State the blood parasite species.
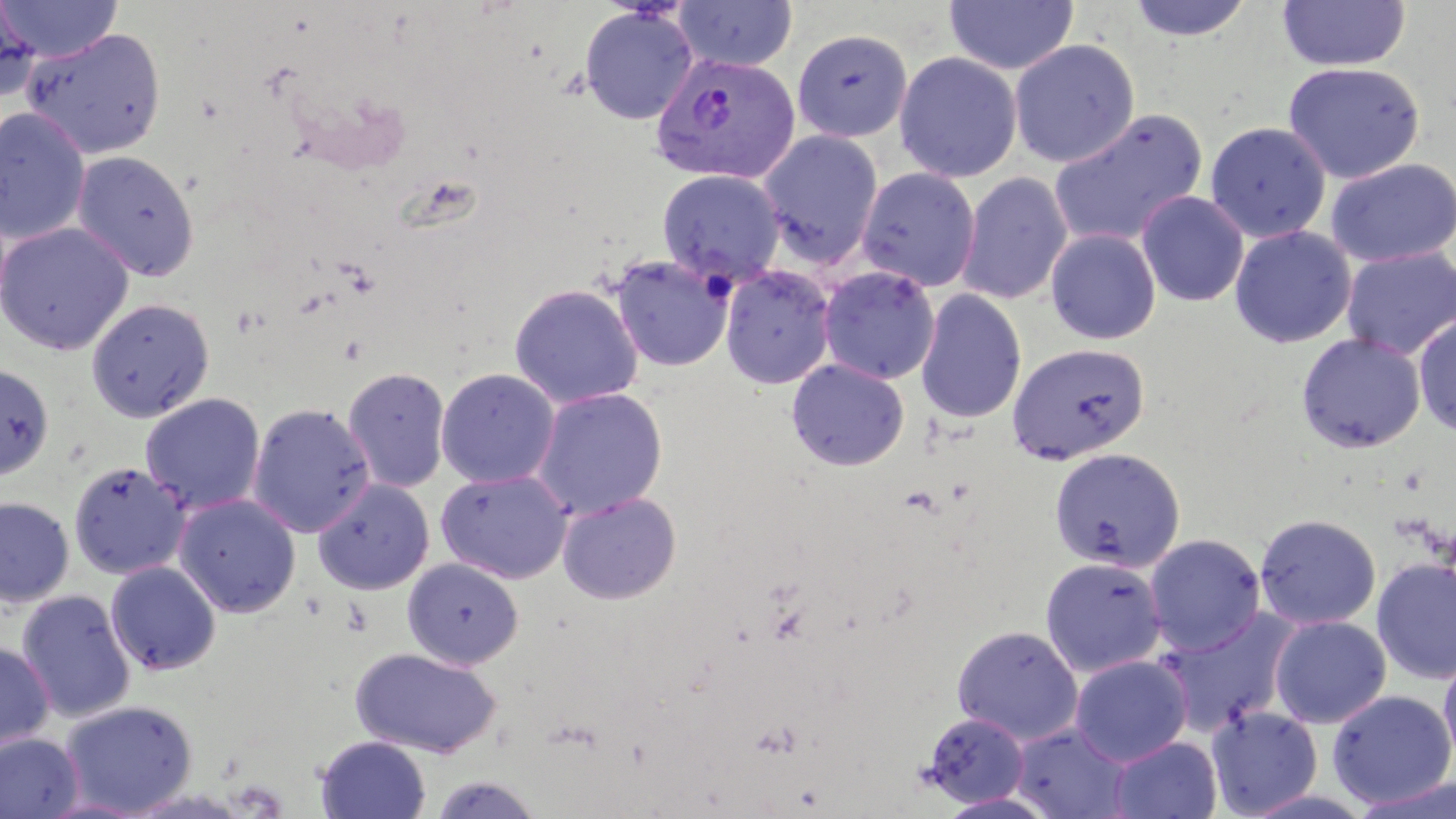

Plasmodium vivax.

Approximate bounding boxes as named x1/y1/x2/y2 corners in pixels. Uninfected red blood cell locations: (x1=1, y1=0, x2=123, y2=64), (x1=943, y1=0, x2=1079, y2=76), (x1=1123, y1=0, x2=1256, y2=42), (x1=1276, y1=0, x2=1410, y2=73), (x1=674, y1=1, x2=798, y2=72), (x1=0, y1=2, x2=40, y2=105), (x1=578, y1=5, x2=700, y2=125), (x1=21, y1=27, x2=167, y2=159), (x1=792, y1=29, x2=912, y2=143), (x1=793, y1=35, x2=1018, y2=166), (x1=1009, y1=38, x2=1140, y2=168), (x1=894, y1=51, x2=1022, y2=183), (x1=1282, y1=62, x2=1425, y2=183), (x1=0, y1=106, x2=90, y2=245), (x1=1048, y1=109, x2=1207, y2=248), (x1=1205, y1=121, x2=1331, y2=243), (x1=758, y1=128, x2=884, y2=268), (x1=71, y1=151, x2=200, y2=281), (x1=1325, y1=157, x2=1456, y2=267), (x1=856, y1=167, x2=981, y2=292), (x1=656, y1=169, x2=786, y2=288), (x1=956, y1=172, x2=1072, y2=306), (x1=1136, y1=191, x2=1249, y2=308), (x1=0, y1=222, x2=134, y2=355), (x1=1229, y1=225, x2=1357, y2=348), (x1=1045, y1=228, x2=1162, y2=345), (x1=1341, y1=246, x2=1456, y2=360), (x1=608, y1=254, x2=735, y2=372), (x1=720, y1=264, x2=836, y2=389), (x1=818, y1=266, x2=940, y2=384), (x1=508, y1=282, x2=644, y2=410), (x1=915, y1=289, x2=1027, y2=424), (x1=85, y1=297, x2=215, y2=424), (x1=1412, y1=313, x2=1456, y2=438), (x1=1295, y1=332, x2=1426, y2=453), (x1=1007, y1=342, x2=1150, y2=464), (x1=786, y1=358, x2=910, y2=471), (x1=0, y1=363, x2=54, y2=480), (x1=342, y1=367, x2=451, y2=493), (x1=436, y1=368, x2=560, y2=489), (x1=531, y1=386, x2=669, y2=520), (x1=140, y1=393, x2=266, y2=515), (x1=247, y1=401, x2=375, y2=538), (x1=1048, y1=447, x2=1186, y2=572), (x1=68, y1=461, x2=190, y2=580), (x1=435, y1=469, x2=572, y2=584), (x1=312, y1=479, x2=435, y2=596), (x1=557, y1=492, x2=682, y2=604), (x1=173, y1=494, x2=302, y2=617), (x1=0, y1=497, x2=74, y2=607), (x1=1254, y1=513, x2=1382, y2=630), (x1=1144, y1=533, x2=1266, y2=657), (x1=1040, y1=556, x2=1168, y2=677), (x1=402, y1=558, x2=524, y2=670), (x1=1371, y1=558, x2=1456, y2=685), (x1=105, y1=561, x2=221, y2=676), (x1=16, y1=589, x2=137, y2=723), (x1=1155, y1=610, x2=1298, y2=736), (x1=1269, y1=615, x2=1392, y2=728), (x1=951, y1=625, x2=1084, y2=744), (x1=0, y1=641, x2=55, y2=754), (x1=349, y1=647, x2=502, y2=758), (x1=1438, y1=650, x2=1456, y2=772), (x1=1070, y1=655, x2=1193, y2=766), (x1=1327, y1=689, x2=1456, y2=809), (x1=60, y1=700, x2=197, y2=816), (x1=1206, y1=705, x2=1323, y2=818), (x1=921, y1=712, x2=1031, y2=808), (x1=1011, y1=723, x2=1132, y2=818), (x1=0, y1=732, x2=83, y2=819), (x1=316, y1=736, x2=431, y2=819), (x1=1109, y1=736, x2=1223, y2=819), (x1=428, y1=772, x2=544, y2=818), (x1=937, y1=791, x2=1057, y2=818). Plasmodium vivax-infected red blood cell locations: (x1=650, y1=51, x2=801, y2=185). Optical microscopy. Thin blood smear. May-Grünwald-Giemsa-stained preparation. Image is 1456×819 pixels. One field of a larger specimen. 1000x magnification.